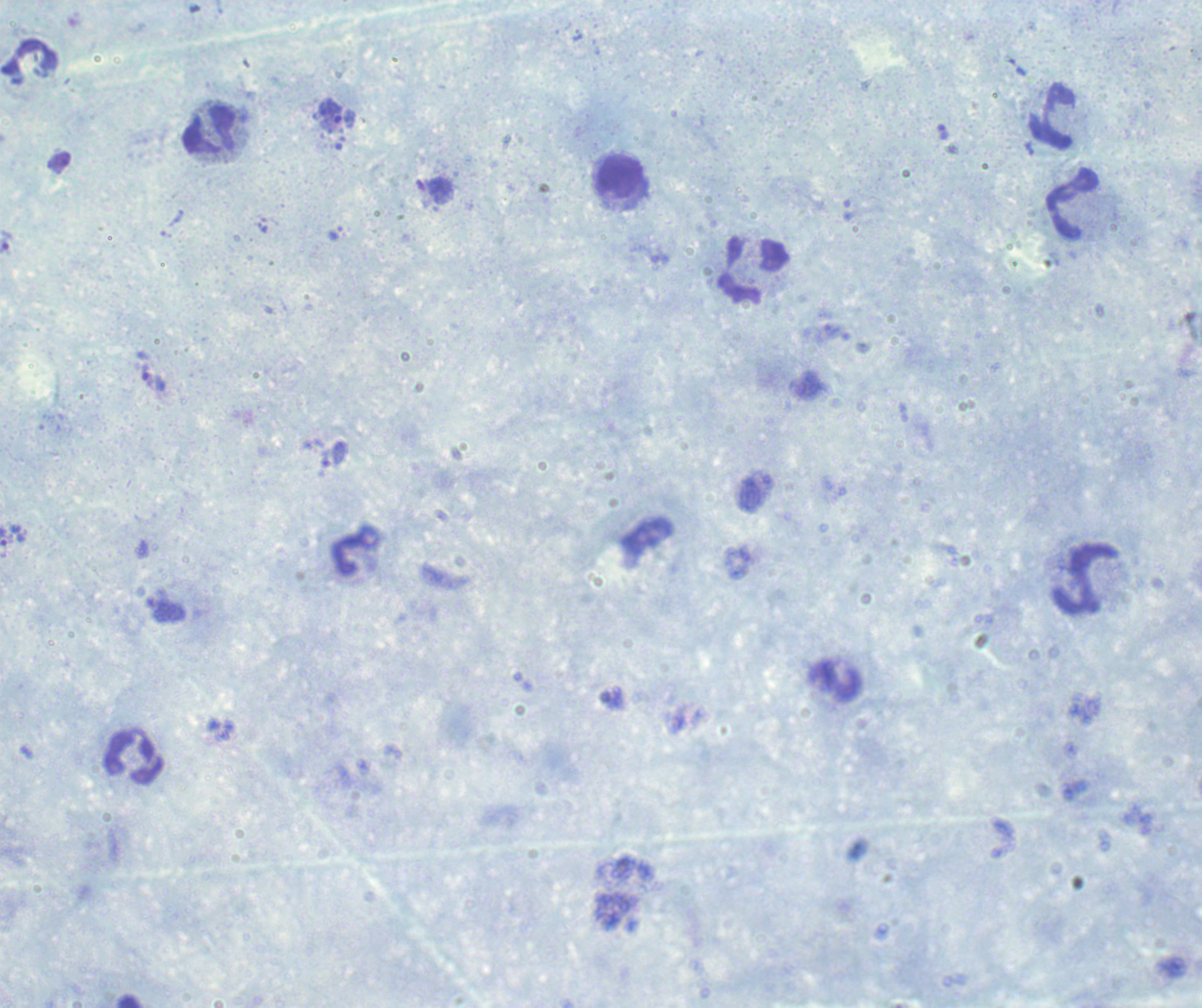

Romanowsky-stained preparation. Thick smear of blood. Single field of view. Image is 1202×1008 pixels.